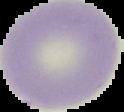
Summary:
  - Image type: segmented cell region on a black background
  - Preparation: thin blood smear
  - Image size: 124×112 pixels
  - Result: negative for malaria parasites